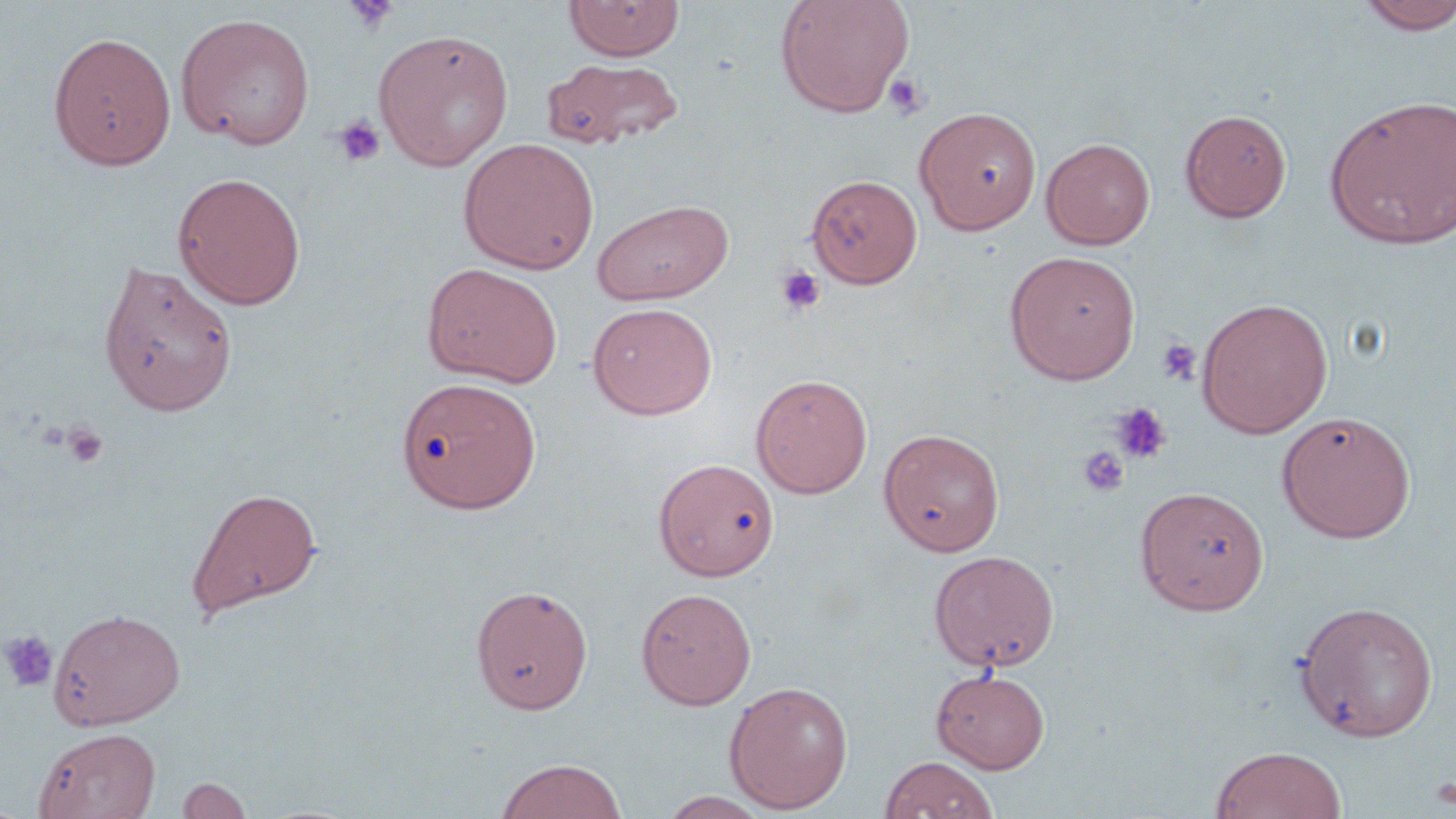

slide-level diagnosis = negative for blood parasites
uninfected red blood cell locations = approximate bounding boxes as named x1/y1/x2/y2 corners in pixels: (x1=563, y1=0, x2=685, y2=61), (x1=774, y1=0, x2=915, y2=116), (x1=1355, y1=1, x2=1456, y2=35), (x1=175, y1=12, x2=316, y2=150), (x1=372, y1=28, x2=514, y2=170), (x1=48, y1=31, x2=177, y2=170), (x1=540, y1=57, x2=684, y2=151), (x1=1323, y1=94, x2=1456, y2=250), (x1=914, y1=106, x2=1041, y2=234), (x1=1179, y1=109, x2=1292, y2=222), (x1=459, y1=137, x2=599, y2=274), (x1=1041, y1=137, x2=1155, y2=250), (x1=172, y1=172, x2=306, y2=309), (x1=807, y1=174, x2=922, y2=288), (x1=591, y1=198, x2=735, y2=305), (x1=1003, y1=250, x2=1141, y2=384), (x1=98, y1=258, x2=239, y2=417), (x1=423, y1=263, x2=563, y2=388), (x1=1196, y1=297, x2=1333, y2=438), (x1=587, y1=303, x2=717, y2=419), (x1=750, y1=374, x2=872, y2=498), (x1=396, y1=377, x2=539, y2=512), (x1=1277, y1=410, x2=1416, y2=543), (x1=879, y1=428, x2=1004, y2=556), (x1=654, y1=458, x2=780, y2=581), (x1=1135, y1=486, x2=1268, y2=615), (x1=186, y1=487, x2=322, y2=619), (x1=928, y1=550, x2=1059, y2=671), (x1=471, y1=584, x2=593, y2=714), (x1=636, y1=588, x2=757, y2=709), (x1=1294, y1=601, x2=1439, y2=742), (x1=49, y1=607, x2=186, y2=730), (x1=930, y1=668, x2=1051, y2=773), (x1=723, y1=680, x2=853, y2=813), (x1=33, y1=727, x2=160, y2=819), (x1=1210, y1=745, x2=1347, y2=819), (x1=880, y1=755, x2=999, y2=819), (x1=495, y1=757, x2=628, y2=819), (x1=177, y1=776, x2=254, y2=818), (x1=658, y1=791, x2=773, y2=818)
modality = light microscopy
field of view = one of a larger specimen
preparation = thin blood smear
stain = May-Grünwald-Giemsa
magnification = 1000x
platelet locations = approximate bounding boxes as named x1/y1/x2/y2 corners in pixels: (x1=344, y1=0, x2=400, y2=34), (x1=883, y1=73, x2=930, y2=120), (x1=334, y1=115, x2=385, y2=167), (x1=774, y1=263, x2=826, y2=317), (x1=1157, y1=339, x2=1200, y2=386), (x1=1110, y1=402, x2=1172, y2=464), (x1=61, y1=422, x2=107, y2=468), (x1=1077, y1=446, x2=1130, y2=498), (x1=0, y1=630, x2=58, y2=692), (x1=1430, y1=774, x2=1456, y2=812)
image size = 1456×819 pixels